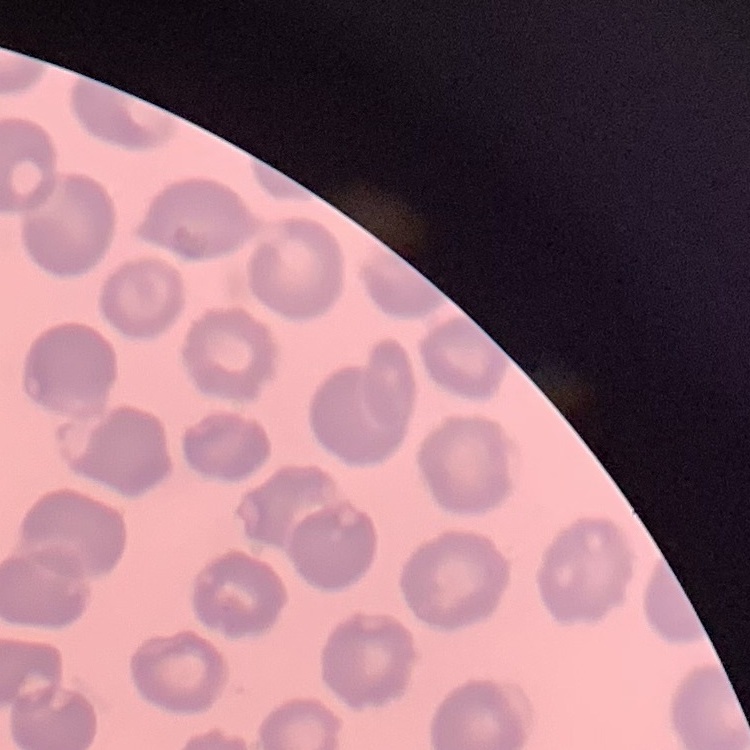
red blood cell morphology = no rouleaux formation
stain = Field's or Giemsa
image type = square crop of a larger photomicrograph
preparation = thin blood smear